Assess this cell for malaria.
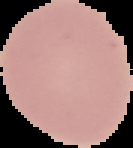
Uninfected.

preparation = thin blood film
image type = segmented cell region with the area outside set to black
image size = 133×148 pixels